Outline each Plasmodium ovale-infected red blood cell.
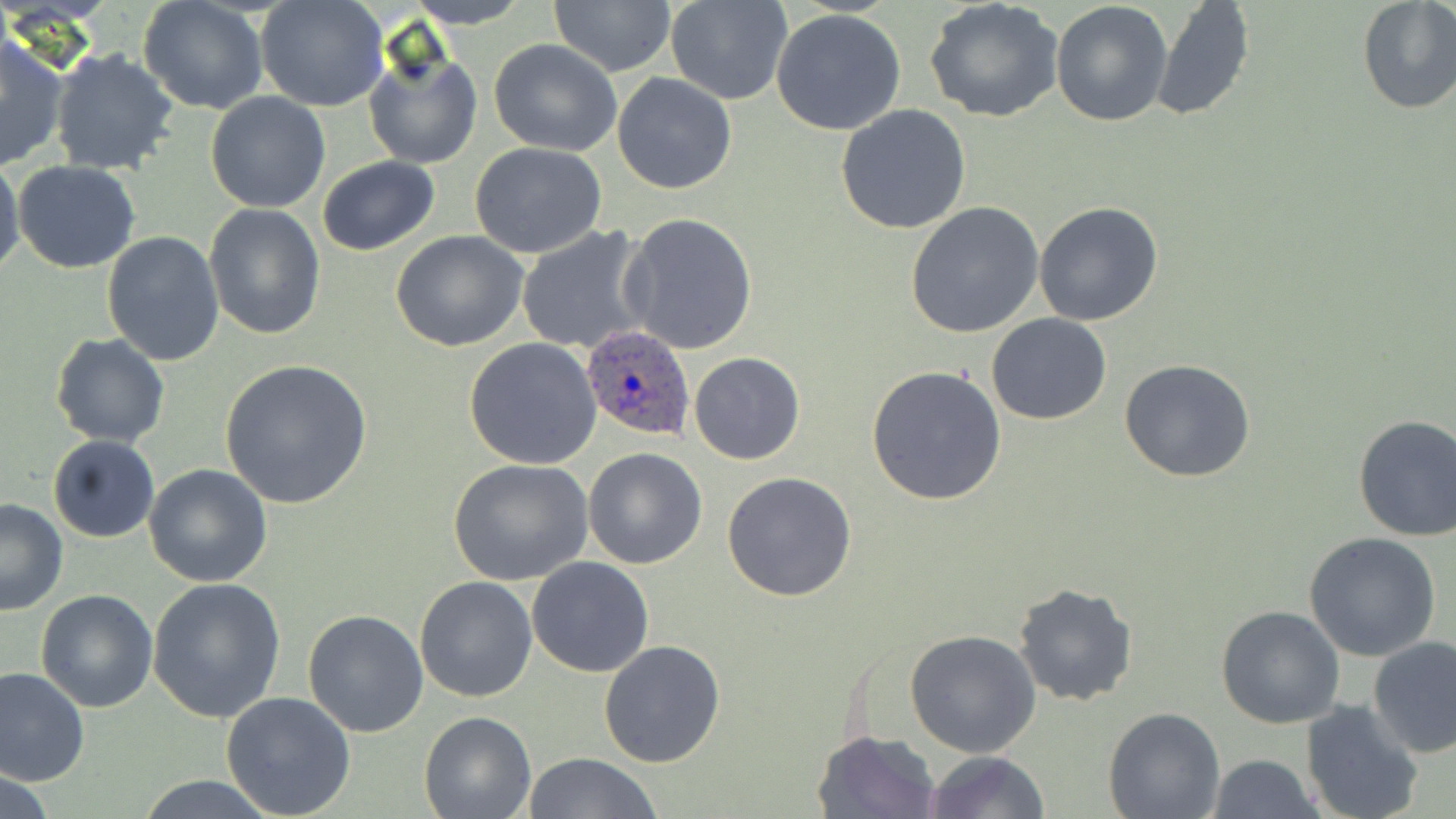
Approximate bounding boxes as (x1,y1)-(x2,y2) corner pairs in pixels.
Plasmodium ovale-infected red blood cells: (579,326)-(696,446).

Summary:
  - Uninfected red blood cell locations: (403,0)-(536,26), (548,0)-(676,77), (667,0)-(792,105), (925,0)-(1064,123), (1356,0)-(1456,116), (256,1)-(389,112), (1050,1)-(1174,128), (1148,1)-(1255,122), (138,2)-(269,114), (772,9)-(907,136), (0,32)-(70,170), (489,39)-(621,154), (364,45)-(483,172), (48,49)-(182,176), (613,72)-(737,195), (204,91)-(330,213), (836,103)-(971,233), (469,143)-(607,257), (0,156)-(25,283), (316,157)-(440,255), (13,161)-(141,274), (1033,201)-(1165,326), (904,202)-(1044,338), (203,203)-(326,339), (620,212)-(759,355), (517,225)-(653,356), (101,231)-(225,367), (390,231)-(531,352), (986,313)-(1112,424), (49,332)-(170,448), (462,337)-(605,469), (688,352)-(806,465), (1120,359)-(1256,482), (220,360)-(373,510), (866,364)-(1007,506), (1352,415)-(1456,541), (46,434)-(161,543), (582,447)-(708,569), (448,458)-(594,587), (143,464)-(272,587), (722,471)-(857,602), (0,498)-(69,615), (1303,533)-(1442,661), (527,557)-(654,677), (414,575)-(539,702), (147,576)-(287,723), (1012,581)-(1138,706), (36,590)-(158,712), (1215,606)-(1345,730), (302,608)-(430,737), (904,629)-(1042,757), (1368,636)-(1456,757), (598,640)-(726,769), (0,665)-(91,786), (220,691)-(355,818), (1300,701)-(1424,819), (1102,707)-(1224,819), (419,711)-(537,819), (813,729)-(941,819), (921,750)-(1052,819), (522,753)-(666,818), (1205,755)-(1326,818), (136,777)-(280,817)
  - Slide-level diagnosis: Plasmodium ovale
  - Preparation: thin blood film
  - Magnification: 1000x
  - Stain: May-Grünwald-Giemsa
  - Field of view: single
  - Image size: 1456×819 pixels
  - Modality: optical microscopy